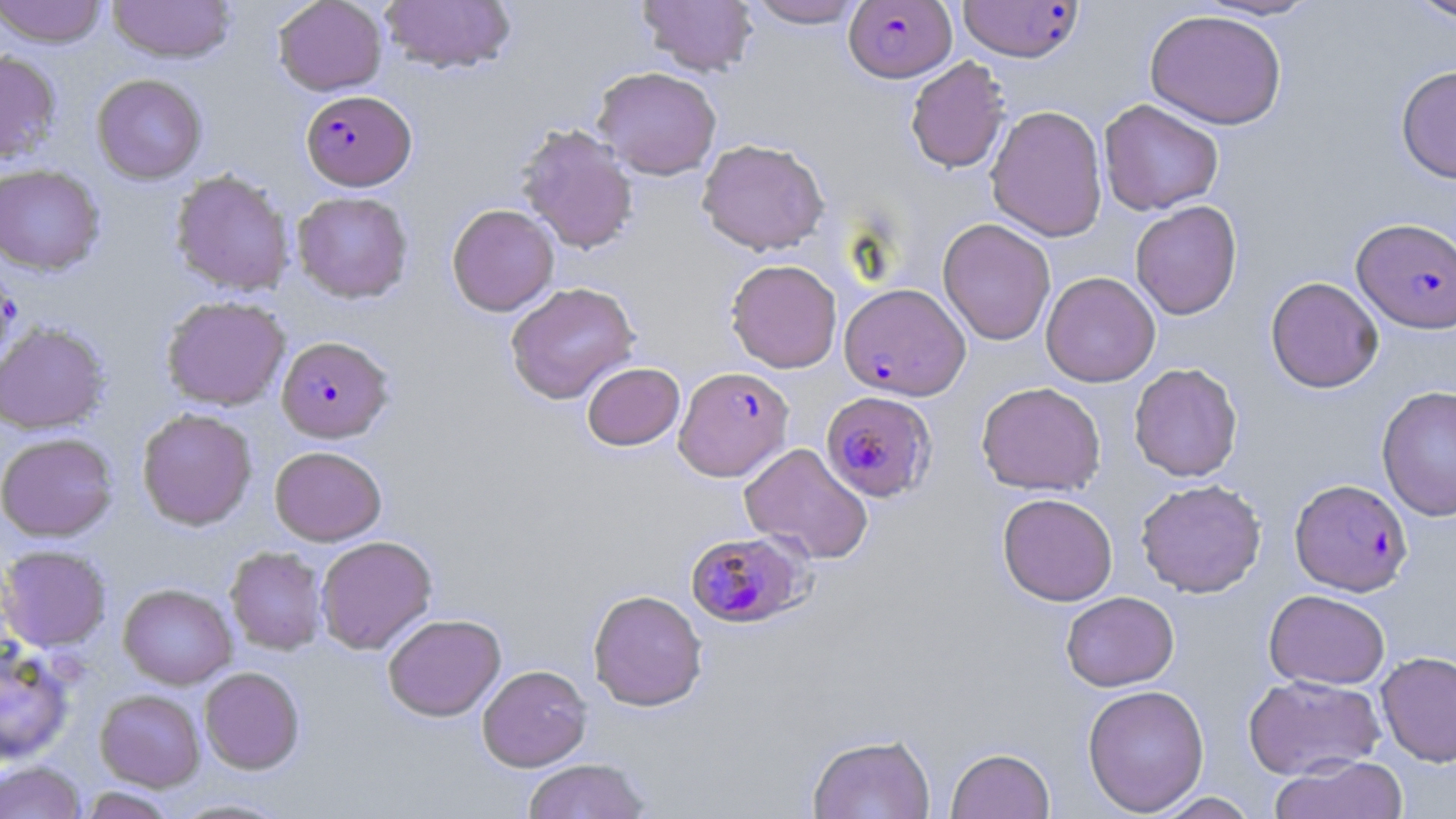
Approximate bounding boxes as [x1, y1, x2, y2] in pixels. Plasmodium falciparum-infected red blood cell locations: [844, 1, 957, 82], [958, 1, 1083, 62], [301, 90, 415, 190], [1352, 217, 1456, 333], [839, 282, 970, 400], [277, 336, 393, 442], [673, 366, 793, 482], [821, 390, 936, 502], [1290, 478, 1413, 596], [684, 530, 809, 628]. Uninfected red blood cell locations: [0, 0, 108, 47], [108, 0, 236, 63], [273, 0, 388, 96], [379, 0, 517, 75], [744, 0, 869, 28], [1193, 0, 1323, 21], [1405, 0, 1456, 23], [637, 1, 758, 77], [1145, 9, 1287, 130], [0, 50, 62, 163], [905, 56, 1011, 174], [1396, 65, 1456, 184], [593, 66, 722, 180], [92, 74, 207, 184], [1098, 99, 1224, 216], [986, 105, 1108, 242], [516, 124, 638, 255], [697, 138, 829, 255], [0, 164, 104, 275], [170, 169, 295, 296], [292, 191, 414, 304], [1130, 200, 1242, 319], [447, 204, 559, 316], [938, 218, 1056, 345], [0, 258, 21, 372], [726, 259, 843, 373], [1041, 271, 1160, 386], [1265, 276, 1384, 393], [505, 281, 639, 404], [161, 295, 290, 411], [0, 322, 110, 434], [582, 362, 685, 450], [1128, 362, 1243, 481], [976, 381, 1106, 496], [1376, 384, 1456, 522], [136, 408, 257, 531], [0, 432, 118, 541], [739, 442, 873, 564], [269, 446, 386, 545], [1136, 479, 1266, 597], [997, 492, 1118, 606], [315, 536, 437, 654], [0, 545, 111, 652], [225, 546, 328, 655], [118, 583, 237, 689], [588, 589, 708, 711], [1264, 589, 1390, 689], [1061, 591, 1179, 691], [383, 613, 506, 721], [0, 640, 75, 765], [1376, 650, 1456, 766], [477, 664, 592, 772], [199, 667, 304, 774], [1243, 673, 1386, 780], [1082, 684, 1210, 815], [95, 689, 205, 790], [807, 733, 935, 819], [946, 747, 1055, 819], [1269, 756, 1409, 819], [521, 758, 652, 819], [1, 760, 85, 819], [76, 787, 180, 818], [1150, 792, 1259, 818], [166, 797, 297, 818]. Slide-level diagnosis: Plasmodium falciparum. May-Grünwald-Giemsa-stained preparation. Captured at 1000x magnification. Single field of view. Thin blood film. Image is 1456×819 pixels. Optical microscopy.